Assess the morphology of the red blood cells.
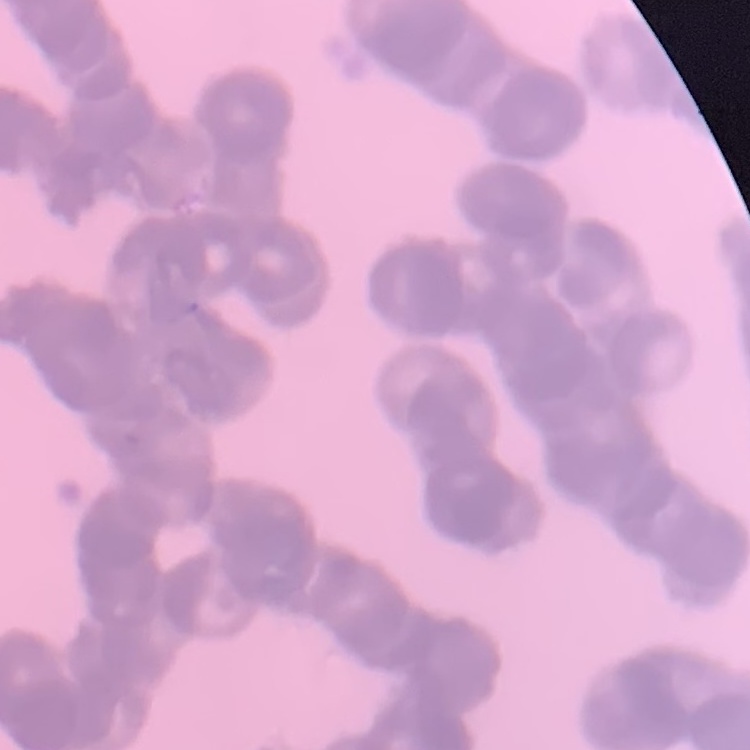
They show rouleaux formation.

Thin peripheral smear. Square crop of a larger photomicrograph. Stained with either Field's or Giemsa.